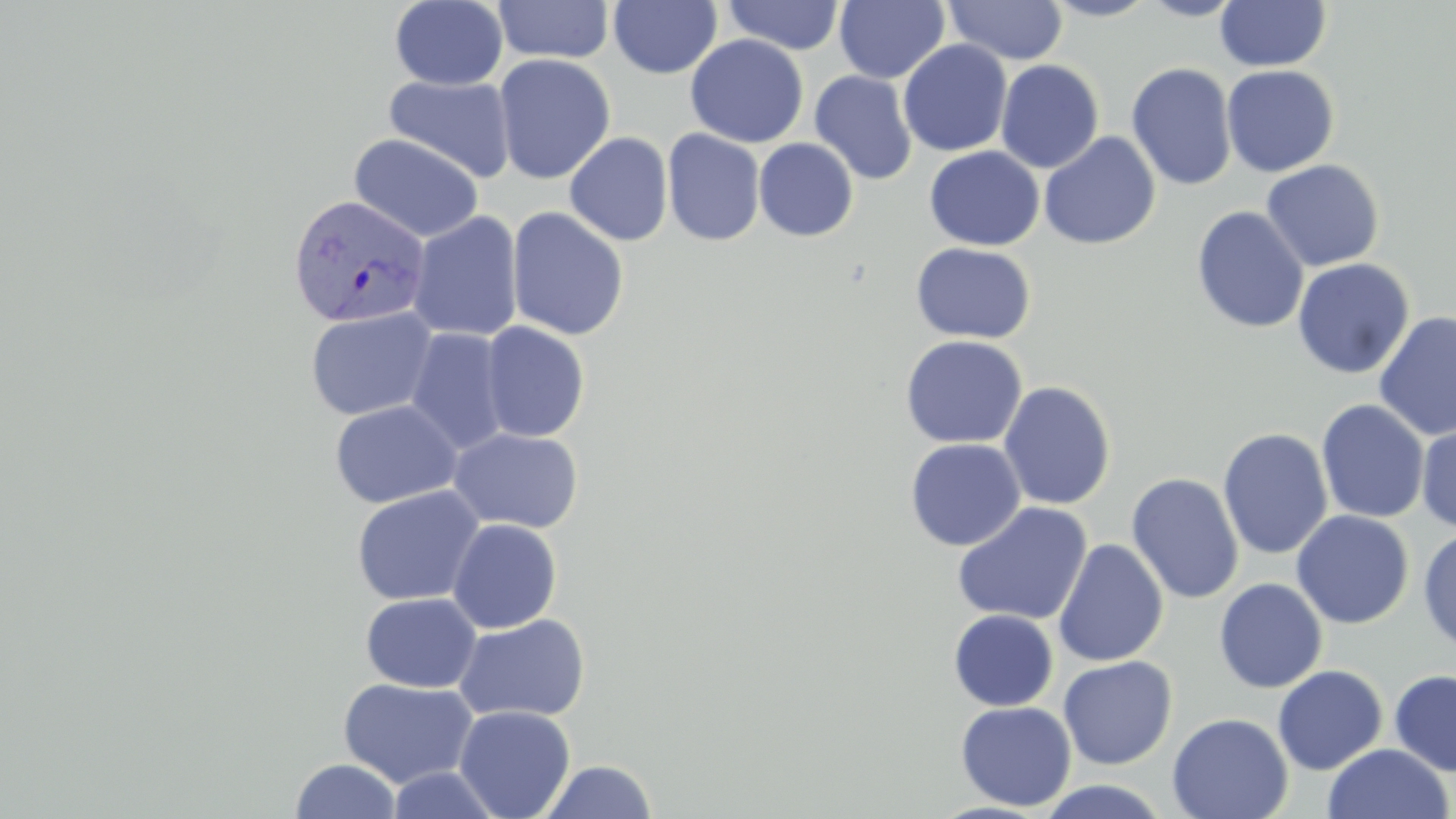

Approximate bounding boxes as (x1, y1, x2, y2) in pixels. Uninfected red blood cell locations: (493, 0, 615, 64), (608, 0, 723, 79), (721, 0, 846, 56), (834, 0, 949, 84), (1041, 0, 1159, 22), (1138, 0, 1247, 21), (389, 1, 508, 90), (944, 1, 1068, 65), (1215, 1, 1332, 72), (685, 34, 808, 148), (898, 39, 1013, 157), (493, 54, 616, 184), (995, 59, 1104, 174), (1126, 62, 1238, 191), (1221, 64, 1339, 177), (809, 70, 918, 186), (384, 74, 516, 183), (662, 128, 766, 247), (564, 132, 673, 246), (1038, 132, 1162, 251), (349, 133, 485, 243), (753, 138, 859, 241), (924, 146, 1044, 251), (1260, 159, 1385, 272), (1191, 205, 1309, 334), (506, 207, 630, 341), (408, 212, 524, 342), (910, 242, 1036, 344), (1292, 258, 1415, 380), (304, 307, 438, 421), (1374, 310, 1456, 442), (479, 321, 590, 442), (405, 328, 512, 455), (899, 335, 1028, 449), (998, 381, 1116, 510), (329, 399, 463, 508), (1316, 399, 1430, 524), (1416, 419, 1456, 534), (448, 427, 584, 534), (1218, 428, 1334, 560), (904, 438, 1026, 551), (1126, 472, 1245, 605), (351, 486, 485, 606), (952, 502, 1093, 626), (1291, 510, 1414, 629), (447, 519, 563, 633), (1418, 526, 1456, 655), (1052, 539, 1169, 667), (1213, 578, 1328, 693), (360, 592, 482, 692), (948, 609, 1059, 711), (452, 613, 591, 724), (1057, 656, 1177, 769), (1273, 665, 1388, 775), (1389, 668, 1456, 777), (338, 678, 479, 788), (955, 701, 1077, 811), (454, 705, 576, 819), (1167, 712, 1293, 819), (1322, 743, 1454, 819), (290, 758, 402, 818), (537, 759, 657, 819), (385, 766, 505, 819), (1035, 779, 1171, 817). Plasmodium vivax-infected red blood cell locations: (287, 193, 431, 329). Slide-level diagnosis: Plasmodium vivax. Captured at 1000x magnification. Thin blood smear. Light microscopy. May-Grünwald-Giemsa-stained preparation. Image is 1456×819 pixels. Single field of view.